Report the malaria status of this cell.
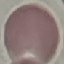
Uninfected.

Summary:
  - Image type: cell patch, automatically extracted from a larger field of view and resized to 64 × 64 pixels
  - Stain: Giemsa
  - Capture: smartphone camera at the microscope eyepiece
  - Preparation: thin blood film